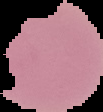

Summary:
  - Image type: cell region segmented out of the field of view; surrounding area masked to black
  - Result: no malaria parasites seen
  - Preparation: thin blood film
  - Image size: 103×112 pixels